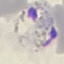
Summary:
  - Result: malaria parasites detected
  - Capture: smartphone through the microscope eyepiece
  - Stain: Giemsa
  - Image type: cell patch, automatically extracted from a larger field of view and resized to 64 × 64 pixels
  - Preparation: thin smear